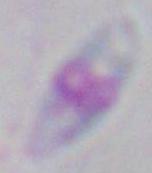
identification = Toxoplasma gondii
modality = photomicrograph
magnification = 1000x